Outline each Trypanosoma brucei.
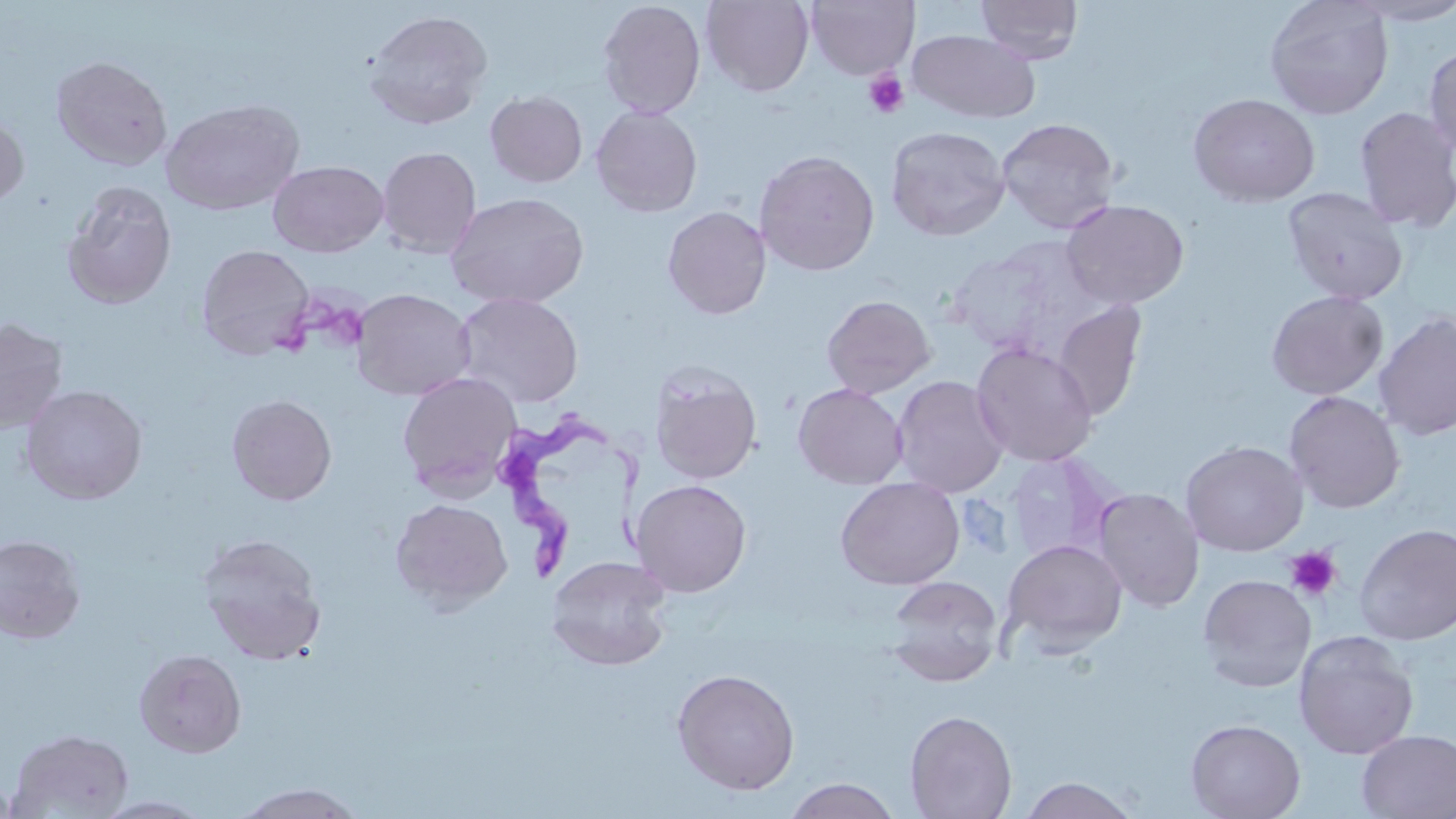
Approximate bounding boxes as (x1, y1, x2, y2) in pixels.
Trypanosoma brucei: (492, 417, 654, 586).

Summary:
  - Platelet locations: (863, 69, 909, 118), (1284, 545, 1343, 602)
  - Uninfected red blood cell locations: (597, 0, 707, 120), (701, 0, 815, 96), (975, 0, 1083, 64), (1264, 0, 1394, 120), (1345, 0, 1456, 26), (805, 1, 919, 80), (362, 8, 495, 131), (908, 29, 1040, 124), (1424, 44, 1456, 160), (51, 55, 173, 171), (485, 90, 588, 188), (1187, 93, 1321, 208), (160, 98, 304, 215), (590, 106, 703, 217), (1353, 106, 1456, 233), (0, 110, 29, 209), (996, 117, 1121, 234), (885, 125, 1010, 241), (377, 146, 482, 259), (754, 149, 880, 276), (267, 160, 390, 258), (62, 181, 178, 309), (1282, 186, 1409, 305), (445, 192, 590, 309), (1060, 198, 1190, 309), (663, 206, 771, 319), (946, 238, 1107, 361), (195, 243, 315, 361), (350, 288, 477, 401), (1266, 289, 1389, 401), (453, 292, 584, 408), (821, 294, 936, 398), (1051, 300, 1147, 421), (1374, 311, 1456, 441), (0, 317, 69, 434), (971, 342, 1099, 467), (649, 364, 762, 484), (397, 371, 523, 498), (890, 375, 1009, 497), (793, 383, 908, 490), (19, 384, 148, 505), (1283, 391, 1405, 513), (226, 394, 337, 505), (1180, 440, 1308, 556), (1005, 451, 1119, 563), (835, 476, 964, 590), (631, 479, 752, 597), (1093, 487, 1205, 611), (390, 498, 513, 611), (1354, 523, 1456, 645), (0, 534, 86, 643), (196, 534, 328, 664), (1003, 538, 1128, 654), (546, 556, 673, 670), (1197, 573, 1317, 693), (885, 575, 1004, 686), (1294, 630, 1419, 759), (133, 649, 247, 759), (671, 668, 800, 795), (904, 710, 1017, 819), (1185, 718, 1305, 819), (6, 727, 134, 818), (1356, 730, 1455, 818), (781, 777, 902, 818), (1017, 777, 1142, 818), (231, 783, 369, 818), (93, 795, 215, 818)
  - Slide-level diagnosis: Trypanosoma brucei
  - Image size: 1456×819 pixels
  - Magnification: 1000x
  - Preparation: thin blood film
  - Stain: May-Grünwald-Giemsa
  - Modality: optical microscopy
  - Field of view: one of a larger specimen